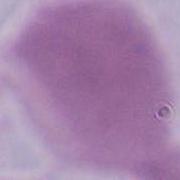
Summary:
  - Modality: micrograph
  - Identification: red blood cell
  - Magnification: 1000x